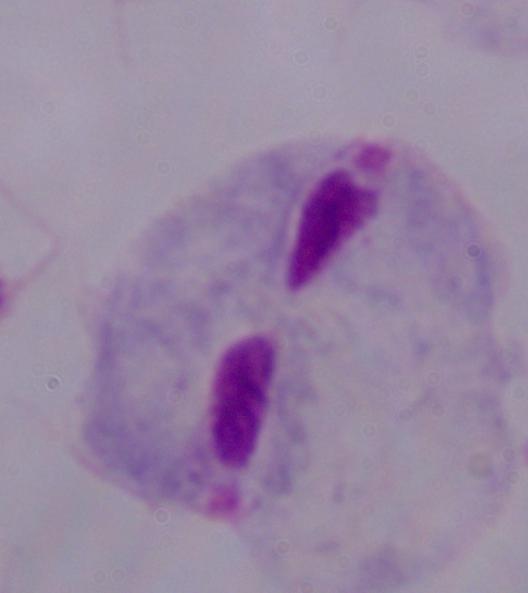

Summary:
  - Identification: trichomonad
  - Modality: micrograph
  - Magnification: 1000x